Give the extent of all Plasmodium malariae-infected red blood cells.
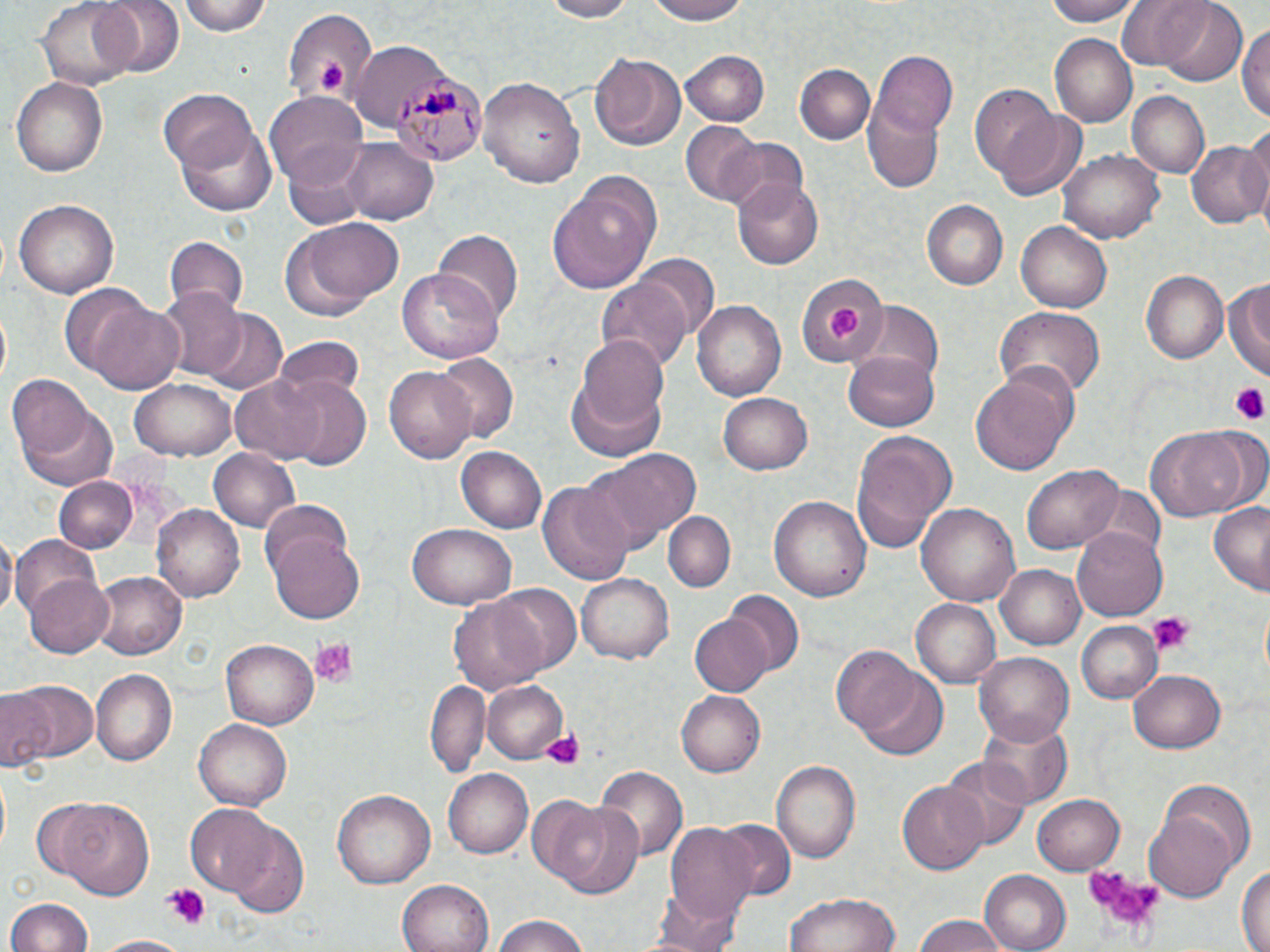

Approximate bounding boxes as named x1/y1/x2/y2 corners in pixels.
Plasmodium malariae-infected red blood cells: (x1=392, y1=69, x2=479, y2=168).

Summary:
  - Uninfected red blood cell locations: (x1=37, y1=0, x2=140, y2=89), (x1=95, y1=0, x2=183, y2=78), (x1=178, y1=0, x2=273, y2=37), (x1=539, y1=0, x2=635, y2=22), (x1=643, y1=0, x2=752, y2=25), (x1=1045, y1=0, x2=1139, y2=26), (x1=1117, y1=0, x2=1215, y2=72), (x1=1150, y1=1, x2=1248, y2=86), (x1=282, y1=9, x2=376, y2=105), (x1=1238, y1=17, x2=1270, y2=127), (x1=1050, y1=36, x2=1135, y2=125), (x1=345, y1=41, x2=436, y2=124), (x1=871, y1=48, x2=956, y2=145), (x1=679, y1=49, x2=769, y2=125), (x1=590, y1=51, x2=688, y2=151), (x1=794, y1=64, x2=875, y2=144), (x1=862, y1=74, x2=949, y2=195), (x1=10, y1=76, x2=108, y2=175), (x1=479, y1=78, x2=585, y2=190), (x1=970, y1=87, x2=1067, y2=189), (x1=264, y1=91, x2=367, y2=185), (x1=1126, y1=91, x2=1210, y2=180), (x1=160, y1=93, x2=270, y2=215), (x1=996, y1=108, x2=1088, y2=201), (x1=680, y1=122, x2=760, y2=204), (x1=718, y1=138, x2=809, y2=215), (x1=1187, y1=138, x2=1268, y2=227), (x1=343, y1=139, x2=437, y2=223), (x1=283, y1=147, x2=371, y2=229), (x1=1063, y1=150, x2=1165, y2=243), (x1=547, y1=172, x2=662, y2=293), (x1=734, y1=180, x2=823, y2=268), (x1=11, y1=200, x2=120, y2=298), (x1=922, y1=201, x2=1006, y2=290), (x1=290, y1=216, x2=405, y2=311), (x1=1015, y1=220, x2=1113, y2=313), (x1=434, y1=229, x2=523, y2=322), (x1=164, y1=237, x2=248, y2=317), (x1=636, y1=254, x2=717, y2=334), (x1=399, y1=268, x2=504, y2=364), (x1=800, y1=270, x2=888, y2=367), (x1=1141, y1=270, x2=1228, y2=363), (x1=1225, y1=275, x2=1269, y2=381), (x1=597, y1=278, x2=691, y2=377), (x1=57, y1=284, x2=155, y2=377), (x1=157, y1=284, x2=246, y2=380), (x1=693, y1=299, x2=786, y2=399), (x1=84, y1=300, x2=185, y2=396), (x1=853, y1=303, x2=944, y2=390), (x1=994, y1=305, x2=1105, y2=400), (x1=202, y1=310, x2=288, y2=395), (x1=0, y1=312, x2=10, y2=386), (x1=577, y1=335, x2=670, y2=438), (x1=273, y1=337, x2=367, y2=407), (x1=843, y1=351, x2=940, y2=431), (x1=434, y1=352, x2=519, y2=443), (x1=384, y1=366, x2=477, y2=464), (x1=970, y1=369, x2=1073, y2=477), (x1=230, y1=375, x2=328, y2=464), (x1=276, y1=375, x2=373, y2=471), (x1=566, y1=377, x2=668, y2=463), (x1=130, y1=379, x2=236, y2=460), (x1=9, y1=382, x2=116, y2=491), (x1=717, y1=394, x2=813, y2=475), (x1=1146, y1=427, x2=1254, y2=521), (x1=846, y1=431, x2=958, y2=552), (x1=455, y1=444, x2=547, y2=533), (x1=208, y1=448, x2=301, y2=532), (x1=588, y1=448, x2=701, y2=552), (x1=1024, y1=464, x2=1123, y2=553), (x1=52, y1=475, x2=141, y2=554), (x1=538, y1=478, x2=635, y2=590), (x1=1088, y1=484, x2=1165, y2=565), (x1=769, y1=495, x2=872, y2=603), (x1=259, y1=498, x2=358, y2=594), (x1=917, y1=503, x2=1020, y2=606), (x1=152, y1=504, x2=245, y2=602), (x1=1209, y1=505, x2=1270, y2=595), (x1=663, y1=511, x2=736, y2=592), (x1=408, y1=524, x2=517, y2=608), (x1=268, y1=528, x2=367, y2=624), (x1=1073, y1=529, x2=1167, y2=619), (x1=0, y1=530, x2=17, y2=621), (x1=11, y1=536, x2=102, y2=624), (x1=995, y1=564, x2=1086, y2=650), (x1=577, y1=569, x2=674, y2=661), (x1=91, y1=571, x2=186, y2=660), (x1=26, y1=572, x2=114, y2=656), (x1=488, y1=584, x2=582, y2=676), (x1=724, y1=591, x2=804, y2=674), (x1=451, y1=595, x2=550, y2=694), (x1=911, y1=598, x2=1002, y2=688), (x1=691, y1=616, x2=771, y2=696), (x1=1073, y1=621, x2=1163, y2=704), (x1=220, y1=640, x2=316, y2=728), (x1=833, y1=647, x2=928, y2=738), (x1=974, y1=649, x2=1075, y2=744), (x1=1129, y1=670, x2=1226, y2=753), (x1=90, y1=671, x2=176, y2=766), (x1=856, y1=673, x2=950, y2=760), (x1=10, y1=678, x2=98, y2=765), (x1=427, y1=679, x2=489, y2=777), (x1=484, y1=681, x2=569, y2=764), (x1=0, y1=688, x2=54, y2=771), (x1=677, y1=689, x2=766, y2=776), (x1=981, y1=718, x2=1072, y2=805), (x1=195, y1=720, x2=292, y2=810), (x1=940, y1=755, x2=1033, y2=850), (x1=772, y1=760, x2=861, y2=863), (x1=595, y1=766, x2=686, y2=861), (x1=442, y1=768, x2=533, y2=858), (x1=899, y1=783, x2=988, y2=874), (x1=330, y1=788, x2=436, y2=890), (x1=1031, y1=793, x2=1124, y2=876), (x1=527, y1=794, x2=610, y2=885), (x1=55, y1=800, x2=154, y2=900), (x1=547, y1=801, x2=645, y2=899), (x1=185, y1=805, x2=279, y2=893), (x1=1143, y1=808, x2=1237, y2=905), (x1=715, y1=819, x2=795, y2=900), (x1=219, y1=820, x2=309, y2=917), (x1=663, y1=821, x2=759, y2=933), (x1=1237, y1=861, x2=1269, y2=952), (x1=979, y1=871, x2=1070, y2=952), (x1=396, y1=879, x2=494, y2=952), (x1=786, y1=891, x2=900, y2=952), (x1=7, y1=897, x2=93, y2=952), (x1=489, y1=912, x2=596, y2=952), (x1=910, y1=915, x2=1014, y2=952), (x1=93, y1=935, x2=189, y2=952)
  - Platelet locations: (x1=316, y1=59, x2=346, y2=94), (x1=827, y1=305, x2=862, y2=342), (x1=1228, y1=385, x2=1267, y2=425), (x1=1148, y1=610, x2=1193, y2=652), (x1=310, y1=638, x2=357, y2=687), (x1=541, y1=727, x2=588, y2=771), (x1=1086, y1=865, x2=1160, y2=939), (x1=164, y1=884, x2=209, y2=927)
  - Slide-level diagnosis: Plasmodium malariae
  - Image size: 1270×952 pixels
  - Field of view: one of a larger specimen
  - Modality: light microscopy
  - Stain: May-Grünwald-Giemsa
  - Magnification: 1000x
  - Preparation: thin blood film